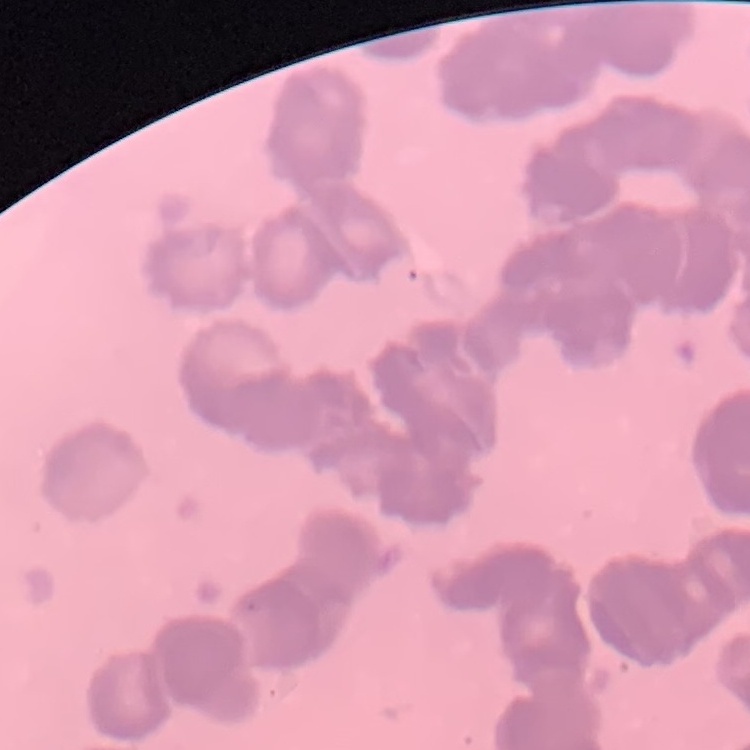 The red blood cells exhibit rouleaux formation. Field's or Giemsa stain. Square crop of a larger photomicrograph. Thin blood smear.